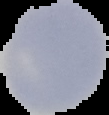

Malaria status: uninfected. From a thin blood smear. Image is 109×115 pixels. The area outside the segmented cell region is set to black.